Classify this cell by malaria status.
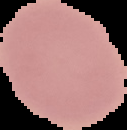
It is uninfected.

Summary:
  - Image type: segmented cell region with the area outside set to black
  - Preparation: thin blood film
  - Image size: 127×130 pixels